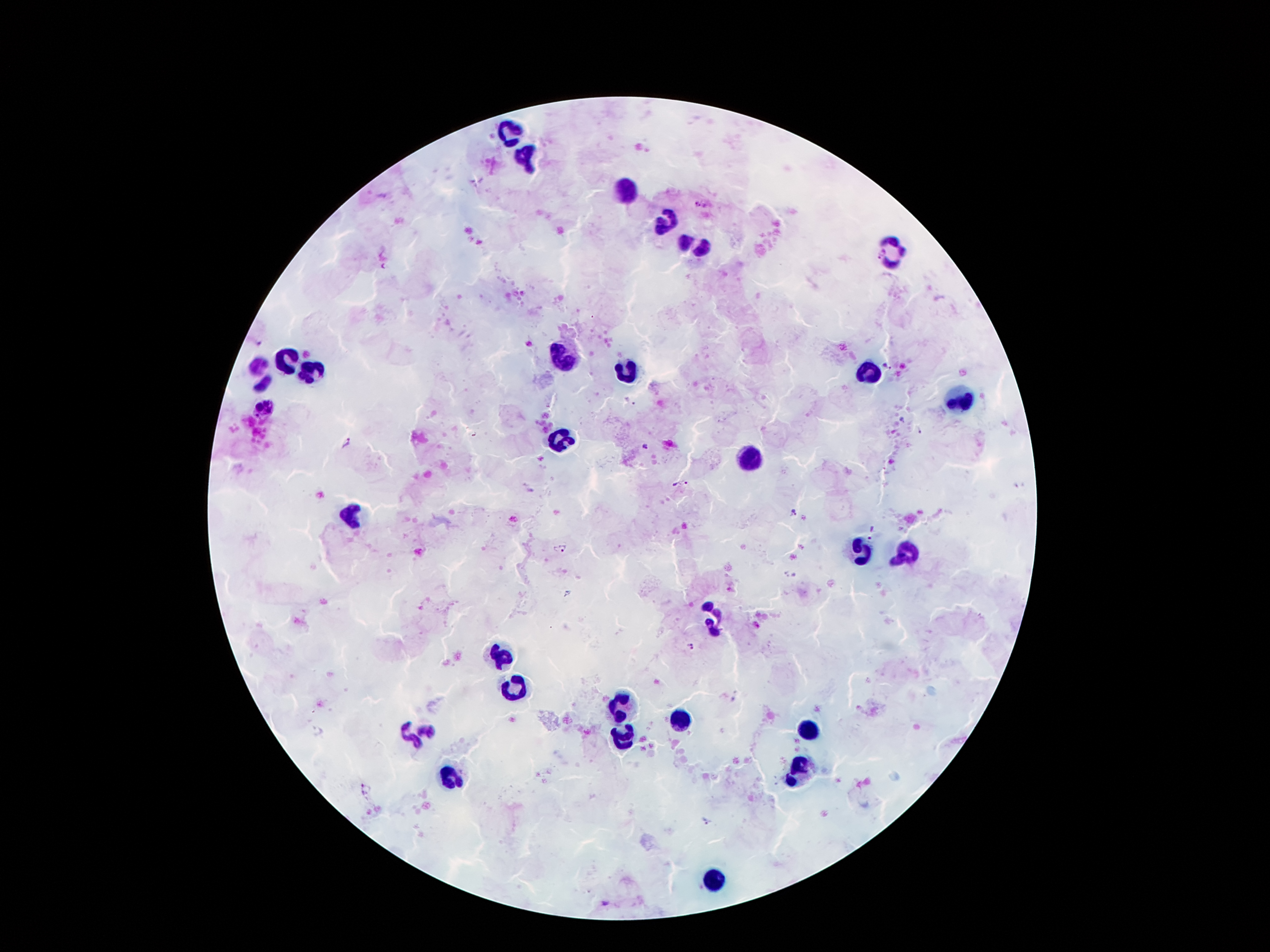

Approximate centers as {x, y} in pixels.
Summary:
  - Malaria parasite locations: {700, 205}, {879, 254}, {889, 367}, {901, 420}, {920, 431}, {345, 442}, {643, 446}, {679, 484}, {793, 510}, {875, 531}, {559, 549}, {692, 646}, {367, 788}, {704, 820}
  - Leukocyte locations: {511, 131}, {527, 157}, {621, 192}, {665, 220}, {693, 243}, {896, 251}, {290, 360}, {565, 362}, {865, 371}, {260, 373}, {311, 373}, {626, 373}, {960, 398}, {560, 442}, {749, 459}, {351, 516}, {861, 553}, {909, 553}, {715, 618}, {502, 654}, {517, 684}, {626, 704}, {682, 721}, {418, 730}, {809, 732}, {624, 738}, {801, 766}, {450, 777}, {713, 880}
  - Magnification: 100x
  - Image size: 1270×952 pixels
  - Stain: Giemsa
  - Preparation: thick blood film
  - Patient malaria status: infected with Plasmodium falciparum
  - Capture: smartphone through the microscope eyepiece
  - Field of view: single